Assess this cell for malaria.
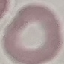

It is uninfected.

Summary:
  - Preparation: thin smear
  - Capture: smartphone through the microscope eyepiece
  - Image type: cell patch, automatically extracted from a larger field of view and resized to 64 × 64 pixels
  - Stain: Giemsa